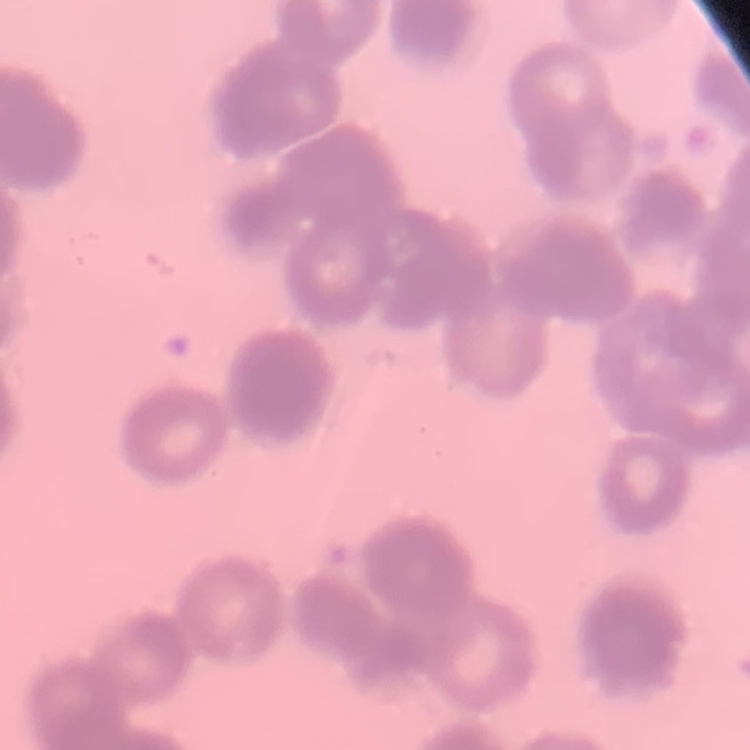
Summary:
  - Red blood cell morphology: rouleaux formation
  - Preparation: thin blood smear
  - Stain: Field's or Giemsa
  - Image type: square crop of a larger photomicrograph